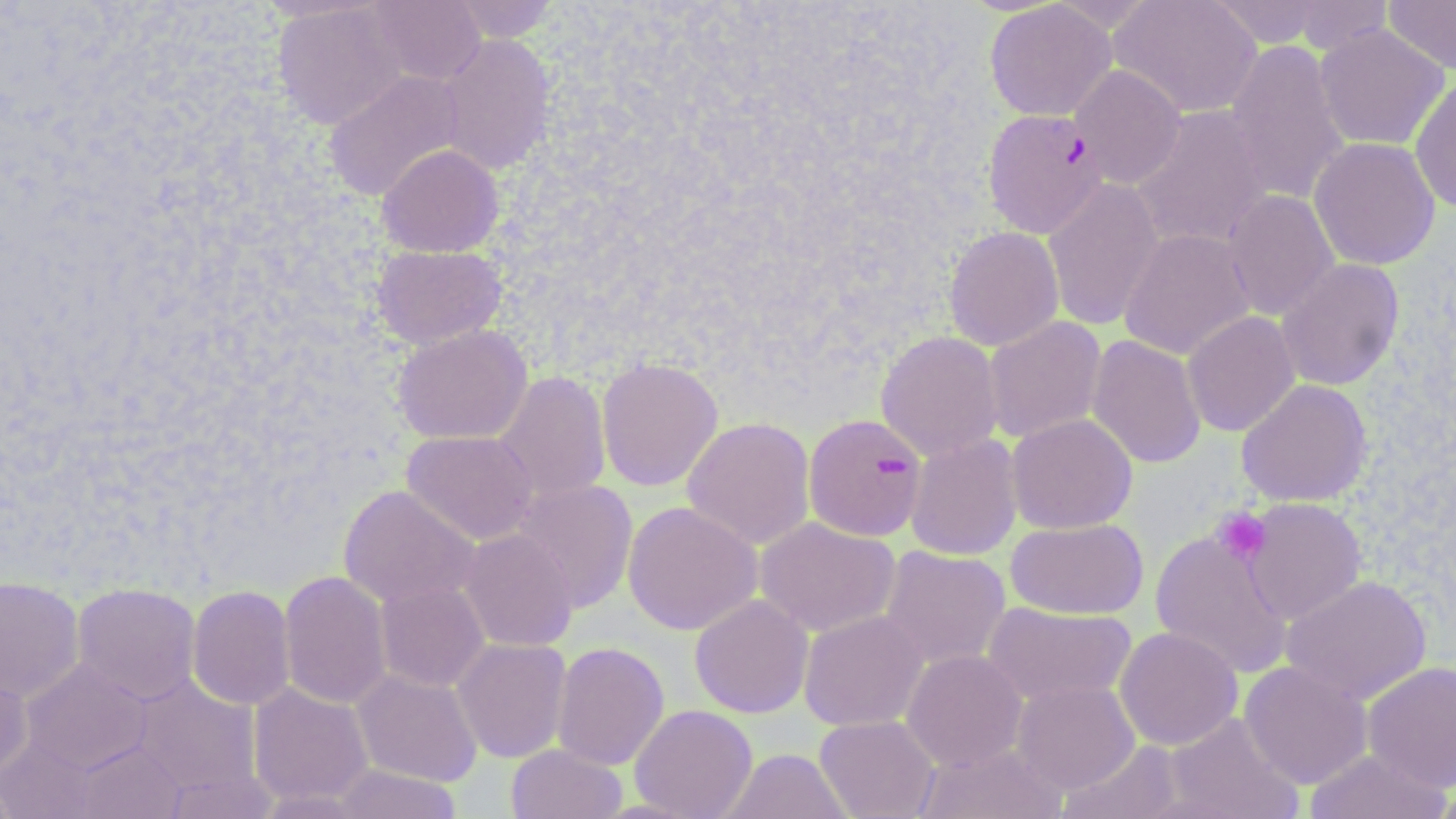
Summary:
  - Coordinate format: approximate bounding boxes as named x1/y1/x2/y2 corners in pixels
  - Plasmodium falciparum-infected red blood cell locations: (x1=982, y1=108, x2=1109, y2=238), (x1=803, y1=413, x2=928, y2=541)
  - Uninfected red blood cell locations: (x1=367, y1=0, x2=485, y2=85), (x1=445, y1=0, x2=561, y2=43), (x1=1109, y1=0, x2=1263, y2=118), (x1=1206, y1=0, x2=1327, y2=48), (x1=1383, y1=0, x2=1456, y2=75), (x1=984, y1=1, x2=1118, y2=121), (x1=1288, y1=1, x2=1393, y2=55), (x1=271, y1=2, x2=407, y2=130), (x1=1313, y1=24, x2=1450, y2=151), (x1=435, y1=34, x2=556, y2=175), (x1=1224, y1=39, x2=1350, y2=205), (x1=1070, y1=65, x2=1186, y2=189), (x1=323, y1=69, x2=465, y2=202), (x1=1409, y1=75, x2=1456, y2=214), (x1=1130, y1=105, x2=1275, y2=251), (x1=1308, y1=136, x2=1441, y2=270), (x1=376, y1=143, x2=504, y2=258), (x1=1043, y1=178, x2=1164, y2=331), (x1=1222, y1=190, x2=1340, y2=320), (x1=944, y1=226, x2=1064, y2=351), (x1=1119, y1=228, x2=1256, y2=360), (x1=371, y1=244, x2=508, y2=350), (x1=1276, y1=258, x2=1405, y2=391), (x1=1182, y1=310, x2=1300, y2=437), (x1=983, y1=316, x2=1107, y2=443), (x1=391, y1=324, x2=532, y2=445), (x1=875, y1=330, x2=1005, y2=461), (x1=1086, y1=335, x2=1206, y2=469), (x1=596, y1=356, x2=724, y2=492), (x1=492, y1=371, x2=612, y2=504), (x1=1236, y1=379, x2=1373, y2=507), (x1=1006, y1=413, x2=1138, y2=534), (x1=681, y1=417, x2=816, y2=550), (x1=402, y1=430, x2=540, y2=545), (x1=905, y1=433, x2=1023, y2=561), (x1=509, y1=479, x2=638, y2=613), (x1=338, y1=484, x2=480, y2=608), (x1=1242, y1=498, x2=1366, y2=625), (x1=622, y1=501, x2=762, y2=636), (x1=755, y1=517, x2=900, y2=637), (x1=1005, y1=517, x2=1148, y2=619), (x1=458, y1=528, x2=579, y2=652), (x1=1150, y1=529, x2=1294, y2=680), (x1=879, y1=546, x2=1011, y2=669), (x1=278, y1=570, x2=393, y2=709), (x1=1281, y1=574, x2=1432, y2=705), (x1=0, y1=575, x2=84, y2=703), (x1=374, y1=581, x2=490, y2=692), (x1=72, y1=582, x2=201, y2=705), (x1=186, y1=585, x2=296, y2=711), (x1=689, y1=595, x2=814, y2=718), (x1=982, y1=602, x2=1138, y2=707), (x1=799, y1=610, x2=929, y2=732), (x1=1114, y1=626, x2=1243, y2=750), (x1=452, y1=637, x2=572, y2=763), (x1=551, y1=641, x2=670, y2=771), (x1=901, y1=649, x2=1028, y2=771), (x1=21, y1=660, x2=152, y2=774), (x1=1239, y1=661, x2=1373, y2=789), (x1=1362, y1=661, x2=1456, y2=792), (x1=0, y1=665, x2=34, y2=780), (x1=351, y1=668, x2=483, y2=787), (x1=130, y1=676, x2=262, y2=796), (x1=1012, y1=680, x2=1139, y2=793), (x1=248, y1=682, x2=374, y2=807), (x1=630, y1=704, x2=758, y2=819), (x1=1162, y1=712, x2=1305, y2=819), (x1=814, y1=714, x2=940, y2=819), (x1=0, y1=737, x2=99, y2=818), (x1=74, y1=740, x2=186, y2=819), (x1=1058, y1=740, x2=1190, y2=819), (x1=916, y1=741, x2=1068, y2=819), (x1=506, y1=744, x2=628, y2=819), (x1=1305, y1=747, x2=1452, y2=819), (x1=719, y1=748, x2=853, y2=819), (x1=330, y1=764, x2=463, y2=819), (x1=0, y1=778, x2=20, y2=818), (x1=1429, y1=781, x2=1456, y2=818)
  - Platelet locations: (x1=1212, y1=507, x2=1271, y2=564)
  - Slide-level diagnosis: Plasmodium falciparum
  - Modality: light microscopy
  - Magnification: 1000x
  - Field of view: single
  - Stain: May-Grünwald-Giemsa
  - Preparation: thin blood smear
  - Image size: 1456×819 pixels